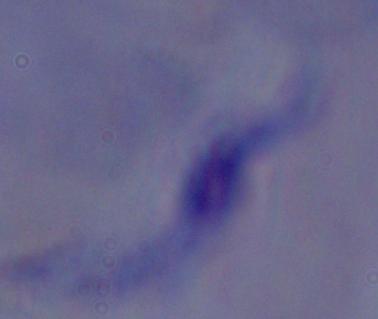

magnification: 1000x
modality: micrograph
identification: trypanosome